Report the malaria status.
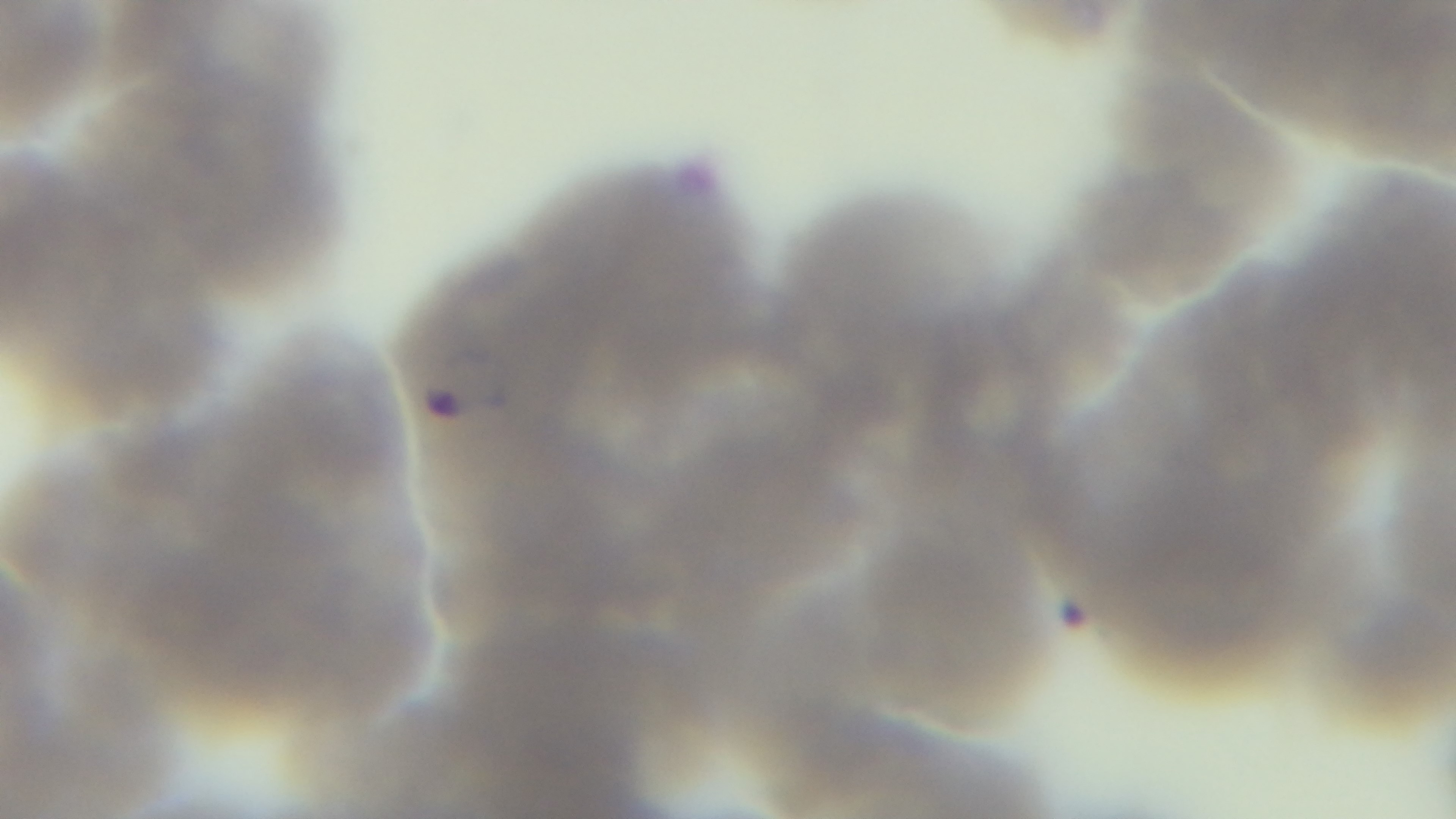
It is infected.

preparation = thin blood film
stain = Giemsa
objective = 100x oil immersion
capture = mounted 4K digital camera
field of view = single
modality = light microscopy